Outline each Plasmodium falciparum-infected red blood cell.
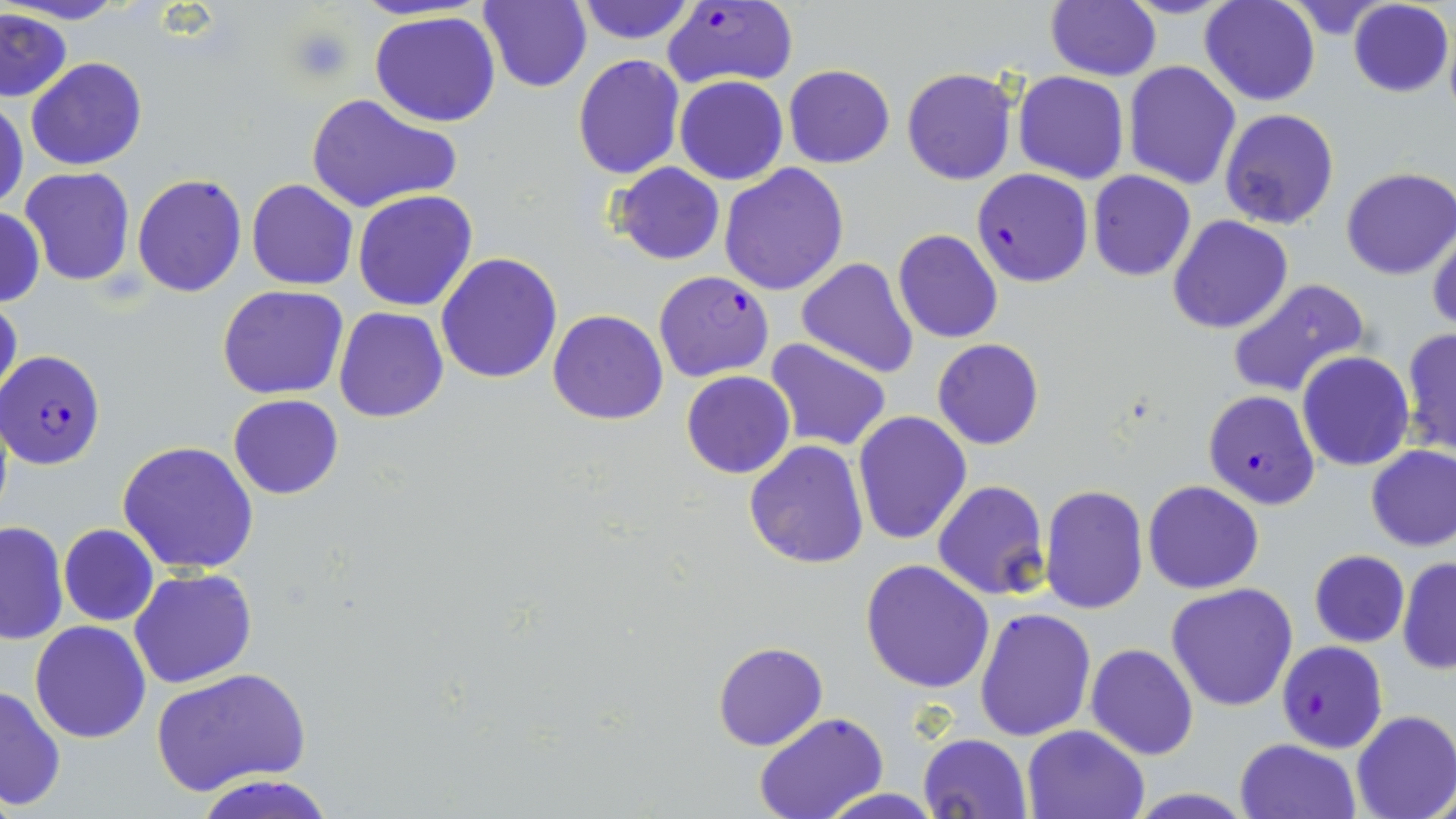
Approximate bounding boxes as named x1/y1/x2/y2 corners in pixels.
Plasmodium falciparum-infected red blood cells: (x1=663, y1=2, x2=799, y2=90), (x1=972, y1=168, x2=1093, y2=286), (x1=653, y1=270, x2=775, y2=382), (x1=2, y1=348, x2=106, y2=469), (x1=1202, y1=389, x2=1320, y2=510), (x1=1278, y1=641, x2=1387, y2=753).

slide-level diagnosis = Plasmodium falciparum
stain = May-Grünwald-Giemsa
platelet locations = approximate bounding boxes as named x1/y1/x2/y2 corners in pixels: (x1=288, y1=26, x2=356, y2=81)
magnification = 1000x
field of view = one of a larger specimen
modality = light microscopy
image size = 1456×819 pixels
preparation = thin blood film
uninfected red blood cell locations = approximate bounding boxes as named x1/y1/x2/y2 corners in pixels: (x1=7, y1=0, x2=124, y2=25), (x1=575, y1=0, x2=696, y2=44), (x1=1199, y1=0, x2=1322, y2=106), (x1=479, y1=1, x2=591, y2=92), (x1=1045, y1=1, x2=1160, y2=81), (x1=1347, y1=1, x2=1454, y2=97), (x1=1, y1=8, x2=74, y2=103), (x1=370, y1=10, x2=502, y2=127), (x1=572, y1=53, x2=685, y2=178), (x1=27, y1=57, x2=146, y2=170), (x1=1123, y1=61, x2=1242, y2=189), (x1=783, y1=64, x2=895, y2=168), (x1=901, y1=67, x2=1017, y2=184), (x1=1013, y1=70, x2=1129, y2=184), (x1=675, y1=76, x2=788, y2=186), (x1=305, y1=91, x2=464, y2=214), (x1=0, y1=94, x2=27, y2=216), (x1=1219, y1=107, x2=1341, y2=230), (x1=718, y1=162, x2=849, y2=296), (x1=609, y1=163, x2=726, y2=265), (x1=19, y1=166, x2=136, y2=288), (x1=1339, y1=168, x2=1455, y2=280), (x1=1087, y1=171, x2=1196, y2=281), (x1=131, y1=172, x2=248, y2=298), (x1=245, y1=178, x2=358, y2=291), (x1=352, y1=190, x2=478, y2=312), (x1=0, y1=207, x2=45, y2=306), (x1=1167, y1=215, x2=1294, y2=334), (x1=1427, y1=219, x2=1456, y2=334), (x1=894, y1=229, x2=1003, y2=343), (x1=436, y1=252, x2=563, y2=384), (x1=796, y1=257, x2=920, y2=379), (x1=1227, y1=278, x2=1371, y2=398), (x1=218, y1=285, x2=348, y2=400), (x1=0, y1=290, x2=22, y2=417), (x1=333, y1=307, x2=448, y2=423), (x1=548, y1=310, x2=668, y2=426), (x1=1400, y1=328, x2=1455, y2=457), (x1=764, y1=338, x2=894, y2=455), (x1=932, y1=338, x2=1042, y2=450), (x1=1297, y1=352, x2=1415, y2=472), (x1=680, y1=370, x2=795, y2=478), (x1=229, y1=395, x2=343, y2=500), (x1=853, y1=409, x2=973, y2=545), (x1=117, y1=440, x2=261, y2=575), (x1=744, y1=441, x2=868, y2=569), (x1=1364, y1=444, x2=1456, y2=552), (x1=1143, y1=480, x2=1264, y2=594), (x1=932, y1=481, x2=1049, y2=601), (x1=1041, y1=483, x2=1149, y2=616), (x1=1, y1=520, x2=68, y2=646), (x1=59, y1=524, x2=159, y2=625), (x1=1309, y1=550, x2=1410, y2=648), (x1=1397, y1=557, x2=1456, y2=673), (x1=860, y1=560, x2=994, y2=693), (x1=128, y1=568, x2=257, y2=689), (x1=1166, y1=583, x2=1299, y2=712), (x1=974, y1=606, x2=1096, y2=742), (x1=29, y1=620, x2=152, y2=744), (x1=712, y1=641, x2=828, y2=750), (x1=1085, y1=642, x2=1199, y2=760), (x1=153, y1=668, x2=309, y2=797), (x1=0, y1=685, x2=66, y2=811), (x1=1352, y1=711, x2=1456, y2=819), (x1=752, y1=712, x2=889, y2=819), (x1=1022, y1=724, x2=1150, y2=817), (x1=917, y1=734, x2=1034, y2=819), (x1=1234, y1=738, x2=1361, y2=819), (x1=197, y1=773, x2=332, y2=819), (x1=822, y1=789, x2=941, y2=819)